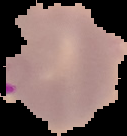

Summary:
  - Image size: 127×136 pixels
  - Preparation: thin blood smear
  - Image type: segmented cell region on a black background
  - Result: malaria parasites detected